Name the blood parasite species.
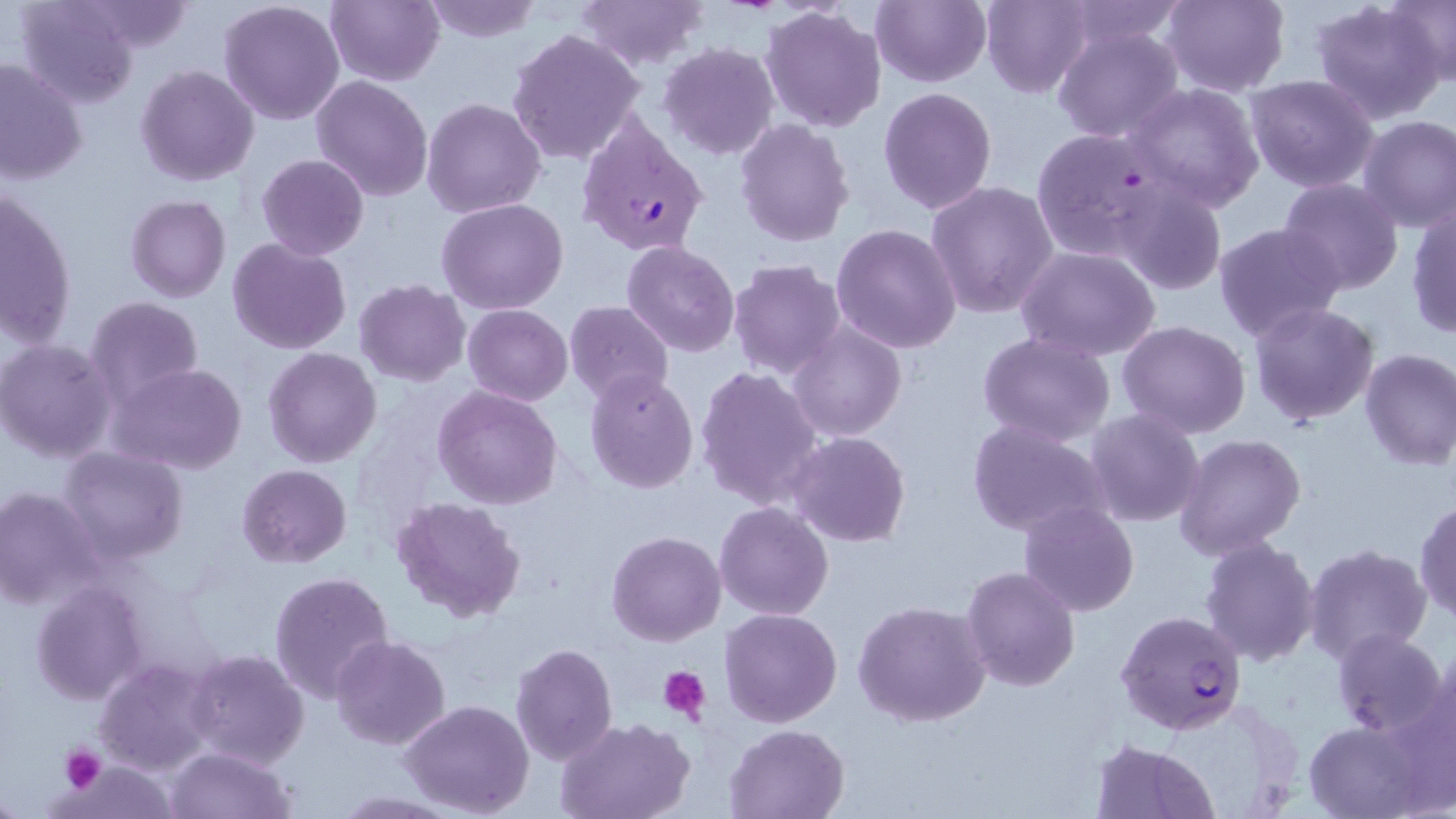
Plasmodium falciparum.

platelet locations = approximate bounding boxes as (x1,y1)-(x2,y2) corner pairs in pixels: (659,666)-(711,720), (61,745)-(106,792)
stain = May-Grünwald-Giemsa
modality = light microscopy
magnification = 1000x
field of view = single
uninfected red blood cell locations = approximate bounding boxes as (x1,y1)-(x2,y2) corner pairs in pixels: (219,0)-(346,124), (325,0)-(443,86), (576,0)-(707,69), (870,0)-(991,88), (981,0)-(1092,99), (1061,0)-(1190,52), (1161,0)-(1290,98), (1310,0)-(1448,125), (1385,0)-(1456,86), (13,1)-(142,108), (72,1)-(197,52), (419,1)-(544,44), (760,6)-(887,133), (1052,24)-(1185,146), (506,27)-(645,164), (659,43)-(779,161), (0,57)-(86,185), (135,64)-(258,185), (1245,74)-(1380,193), (312,76)-(434,203), (1125,82)-(1266,213), (879,86)-(997,214), (422,98)-(547,219), (1357,115)-(1456,232), (735,118)-(855,248), (257,153)-(369,260), (1277,177)-(1405,293), (1110,181)-(1226,296), (925,182)-(1060,320), (126,195)-(231,303), (436,197)-(570,313), (0,198)-(76,350), (1407,206)-(1455,338), (1212,222)-(1347,345), (831,224)-(963,354), (622,239)-(741,357), (228,240)-(350,355), (1014,244)-(1162,363), (728,259)-(848,382), (354,280)-(470,385), (85,296)-(203,410), (564,300)-(675,404), (1249,300)-(1379,427), (463,304)-(572,405), (1118,321)-(1251,439), (788,322)-(907,440), (977,331)-(1116,446), (2,339)-(118,462), (263,346)-(381,467), (1358,349)-(1456,472), (108,363)-(248,476), (694,365)-(825,511), (584,371)-(699,494), (432,384)-(563,511), (1084,409)-(1207,528), (965,419)-(1112,539), (785,431)-(910,548), (1175,432)-(1306,560), (60,447)-(186,565), (238,463)-(351,567), (1,486)-(106,611), (391,496)-(527,622), (1414,497)-(1456,623), (1018,500)-(1140,617), (714,501)-(835,621), (606,529)-(727,645), (1199,536)-(1321,666), (1303,543)-(1433,667), (961,566)-(1081,690), (269,570)-(396,705), (31,581)-(149,705), (853,598)-(991,727), (720,607)-(842,727), (1333,627)-(1446,736), (332,635)-(451,750), (510,643)-(618,765), (184,648)-(308,768), (95,658)-(216,775), (400,700)-(534,818), (558,717)-(699,819), (1302,719)-(1434,819), (725,723)-(850,819), (1090,738)-(1216,818), (164,745)-(293,819), (52,758)-(180,819)
Plasmodium falciparum-infected red blood cell locations = approximate bounding boxes as (x1,y1)-(x2,y2) corner pairs in pixels: (578,118)-(710,257), (1031,128)-(1166,260), (1117,609)-(1245,735)
preparation = thin blood smear
image size = 1456×819 pixels